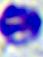

Summary:
  - Magnification: 400x
  - Identification: leukocyte
  - Modality: micrograph